Identify the parasite.
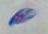

Toxoplasma gondii.

Photomicrograph. Captured at 1000x magnification.